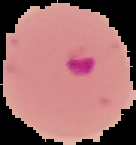
From a thin blood smear. The area outside the segmented cell region is set to black. Result: Plasmodium parasites detected. Image is 136×145 pixels.